Assess the morphology of the red blood cells.
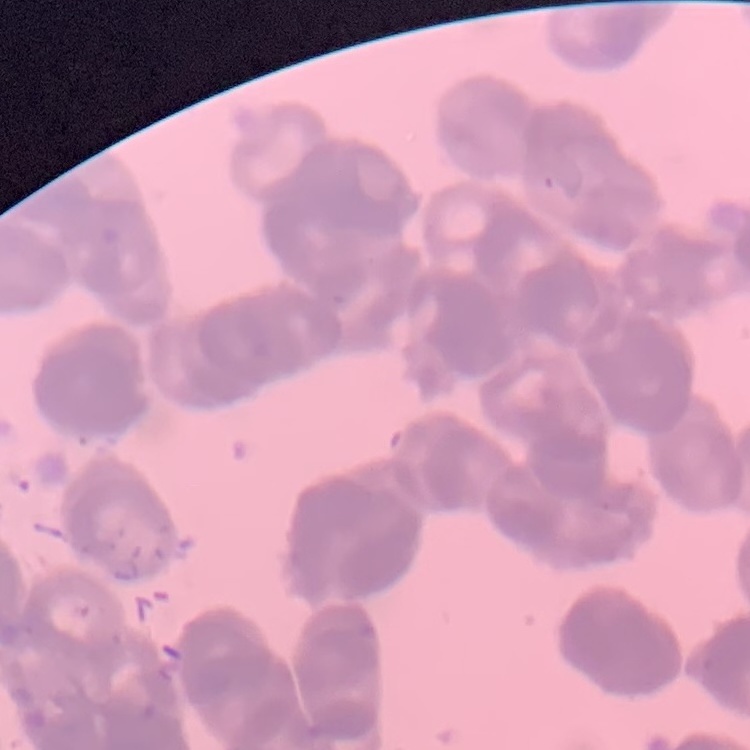
Rouleaux formation.

Summary:
  - Stain: Field's or Giemsa
  - Image type: square crop of a larger photomicrograph
  - Preparation: thin peripheral smear